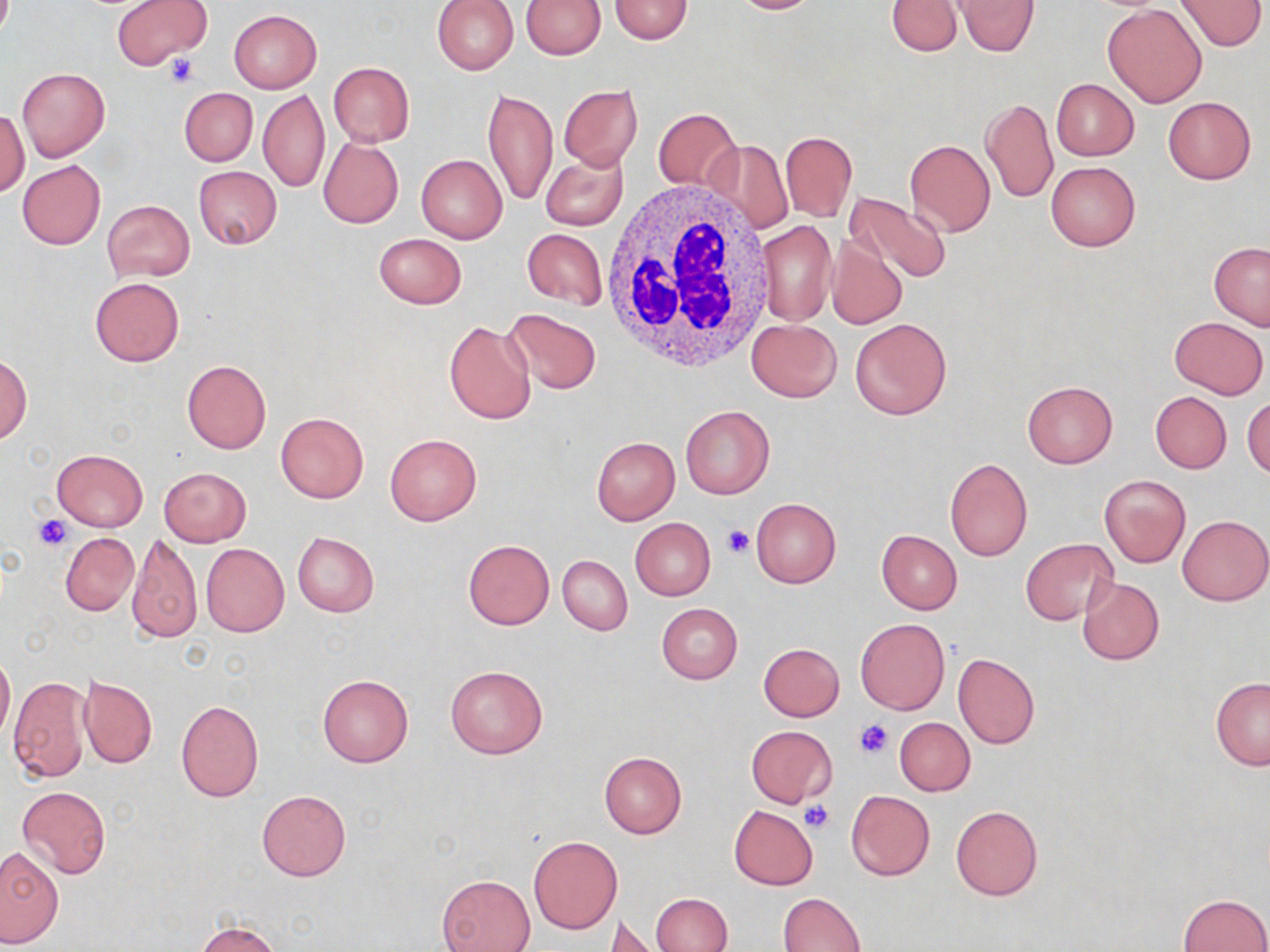 Approximate bounding boxes as [x1, y1, x2, y2] in pixels. White blood cell locations: [599, 179, 778, 373]. Platelet locations: [163, 54, 200, 88], [35, 515, 73, 550], [722, 524, 754, 558], [855, 718, 895, 760], [800, 802, 834, 834]. Uninfected red blood cell locations: [113, 0, 209, 68], [432, 0, 518, 74], [609, 0, 694, 45], [723, 0, 821, 14], [885, 0, 964, 56], [952, 0, 1039, 57], [1175, 0, 1267, 51], [520, 1, 605, 59], [1102, 3, 1207, 107], [229, 10, 322, 93], [327, 61, 415, 147], [17, 67, 110, 162], [1051, 78, 1140, 161], [559, 85, 643, 170], [179, 88, 257, 165], [483, 88, 557, 208], [258, 89, 329, 191], [1163, 96, 1256, 183], [981, 97, 1058, 205], [0, 108, 29, 197], [654, 108, 742, 195], [781, 131, 858, 223], [318, 138, 403, 229], [705, 139, 792, 233], [904, 140, 995, 237], [541, 150, 629, 230], [417, 154, 508, 243], [18, 161, 105, 249], [1045, 161, 1141, 251], [194, 166, 282, 249], [844, 192, 952, 283], [102, 199, 195, 281], [756, 220, 836, 326], [522, 229, 607, 309], [373, 234, 466, 309], [827, 238, 906, 329], [1209, 242, 1270, 331], [91, 277, 183, 367], [502, 308, 602, 394], [1170, 316, 1268, 399], [849, 317, 951, 420], [747, 318, 841, 402], [443, 320, 537, 426], [1, 356, 31, 445], [181, 360, 272, 454], [1022, 380, 1117, 468], [1150, 391, 1231, 473], [1244, 396, 1270, 479], [680, 405, 775, 499], [275, 411, 368, 502], [385, 434, 481, 525], [592, 437, 679, 524], [52, 448, 148, 530], [945, 457, 1033, 560], [159, 467, 251, 546], [1100, 474, 1190, 567], [751, 497, 840, 589], [1177, 515, 1270, 606], [630, 518, 715, 600], [876, 530, 962, 614], [61, 532, 137, 615], [292, 532, 379, 616], [128, 533, 202, 644], [1020, 538, 1121, 627], [464, 539, 554, 629], [201, 543, 289, 637], [558, 554, 633, 636], [1077, 577, 1164, 665], [656, 603, 743, 684], [855, 618, 949, 714], [758, 642, 845, 722], [0, 649, 14, 745], [953, 652, 1040, 748], [445, 665, 548, 759], [78, 673, 158, 768], [9, 675, 90, 782], [317, 675, 413, 768], [1211, 677, 1270, 770], [175, 700, 263, 802], [894, 718, 975, 795], [746, 725, 837, 808], [599, 751, 687, 838], [17, 786, 111, 879], [257, 790, 351, 882], [846, 791, 935, 880], [728, 805, 818, 890], [950, 805, 1043, 900], [529, 836, 622, 933], [0, 848, 64, 947], [438, 874, 535, 952], [779, 892, 867, 952], [649, 893, 733, 952], [1179, 893, 1269, 952], [607, 914, 663, 950], [196, 920, 280, 952]. Slide-level diagnosis: no evidence of blood parasites. Captured at 1000x magnification. Image is 1270×952 pixels. Thin blood smear. Light microscopy. May-Grünwald-Giemsa stain. One field of a larger specimen.